Classify this cell by malaria status.
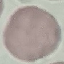
It is uninfected.

Summary:
  - Image type: automatically extracted cell patch, resized to 64 × 64 pixels
  - Preparation: thin smear
  - Capture: smartphone camera at the microscope eyepiece
  - Stain: Giemsa